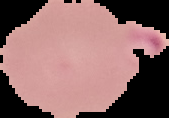
{
  "preparation": "thin blood film",
  "image_type": "cell region segmented out of the field of view; surrounding area masked to black",
  "malaria_status": "parasitized",
  "image_size": "169×118 pixels"
}